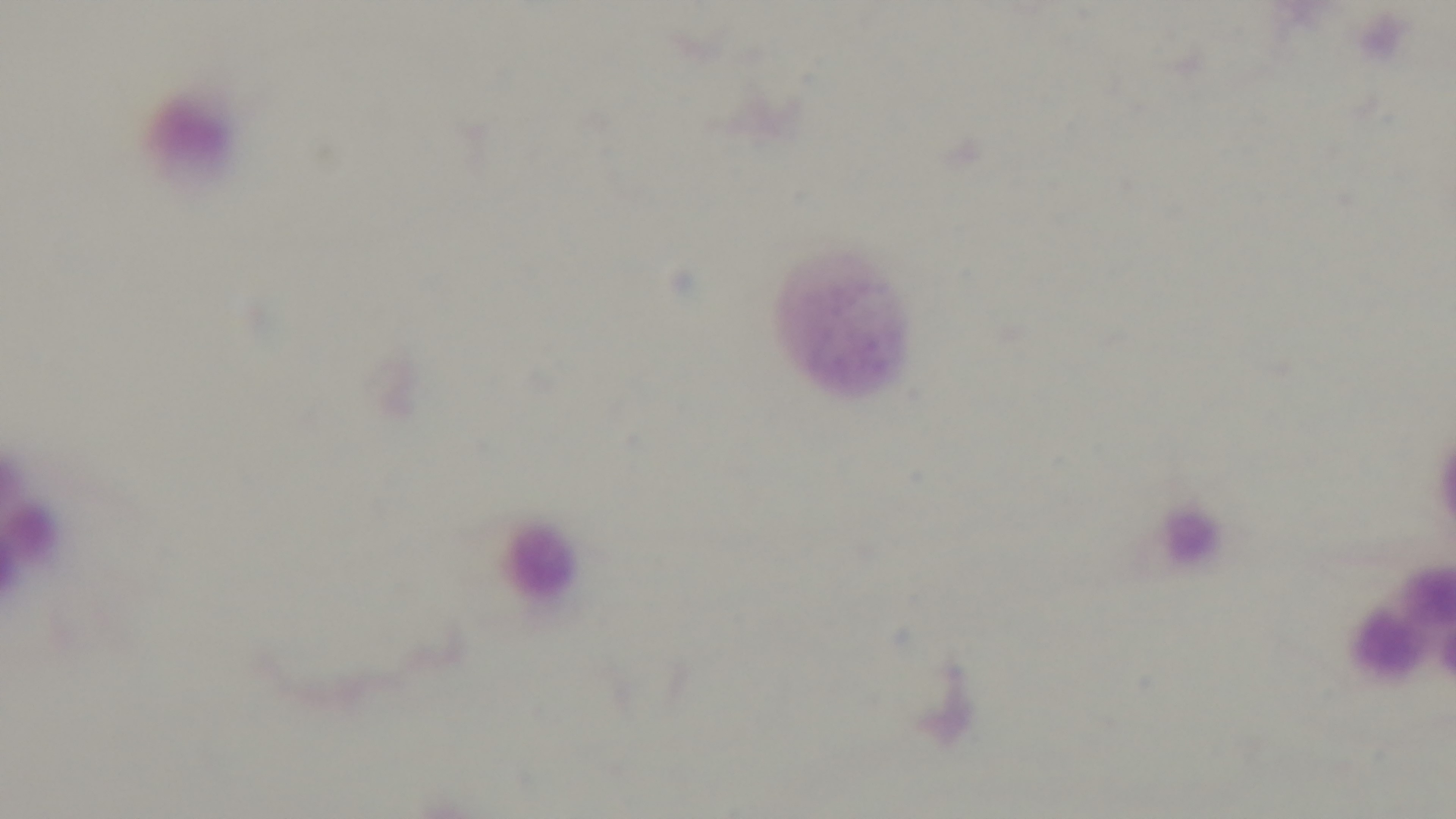
capture = mounted 4K digital camera
objective = 100x oil immersion
malaria status = uninfected
stain = Giemsa
modality = light microscopy
field of view = single
preparation = thick smear